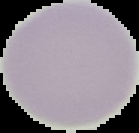
image size = 139×133 pixels
image type = segmented cell region on a black background
preparation = thin blood film
result = negative for Plasmodium parasites